Locate every Plasmodium parasite.
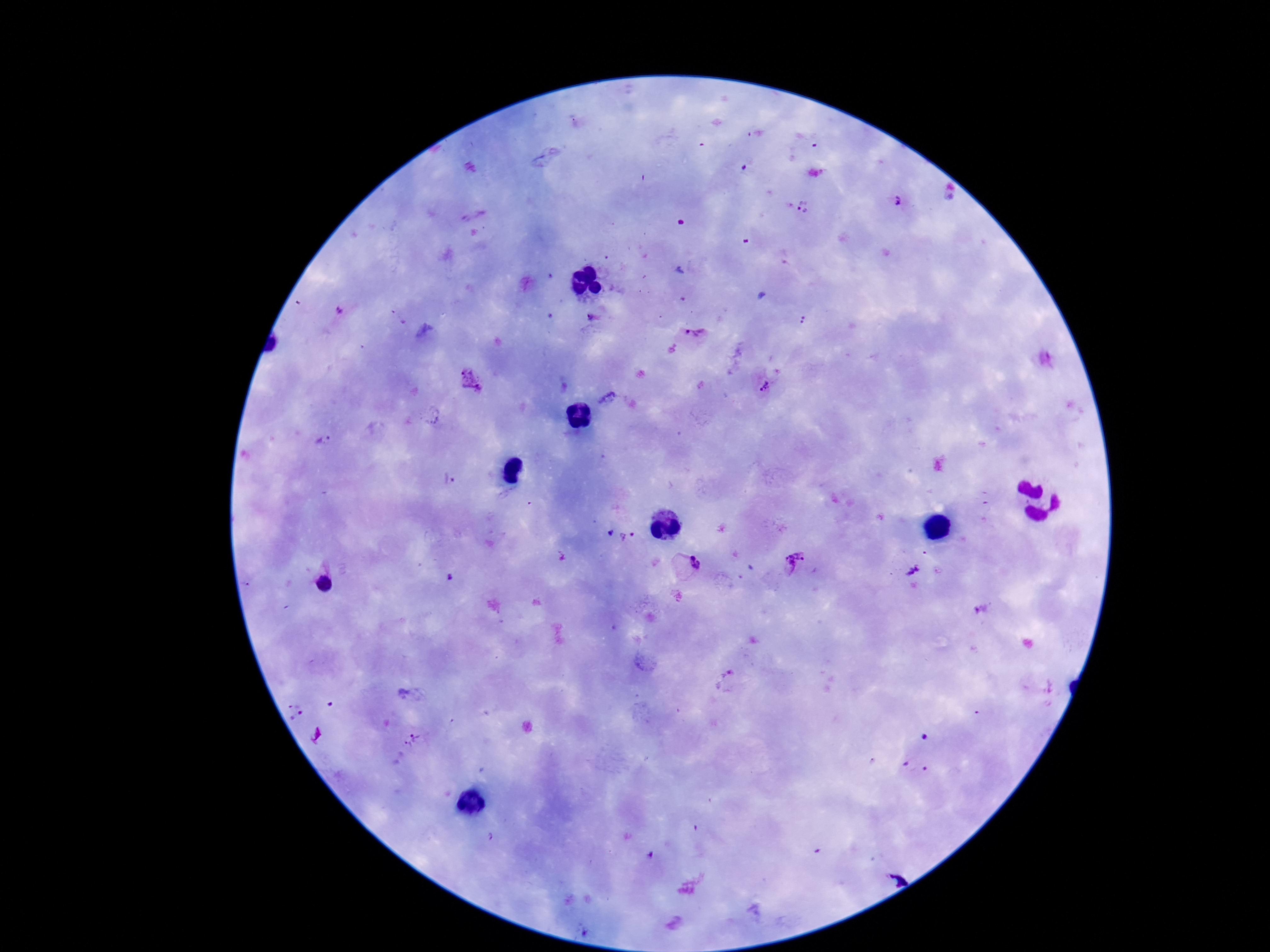
Approximate centers as (x, y) in pixels.
Plasmodium parasites: (744, 168), (896, 200), (804, 207), (339, 309), (592, 317), (694, 334), (471, 381), (761, 386), (607, 398), (323, 441), (450, 479), (609, 533), (632, 534), (623, 538), (794, 563), (695, 565), (912, 571), (324, 584), (981, 609), (730, 672), (297, 711), (923, 737), (413, 741), (911, 765), (925, 769), (491, 837), (650, 855).

Summary:
  - Image size: 1270×952 pixels
  - Magnification: 100x
  - Field of view: single
  - Stain: Giemsa
  - Capture: smartphone camera through the microscope eyepiece
  - Patient malaria status: infected
  - Preparation: thick peripheral-blood smear